Report the malaria status of this cell.
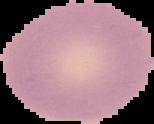

It is uninfected.

preparation = thin blood film
image type = segmented cell region with the area outside set to black
image size = 154×124 pixels